Outline each uninfected red blood cell.
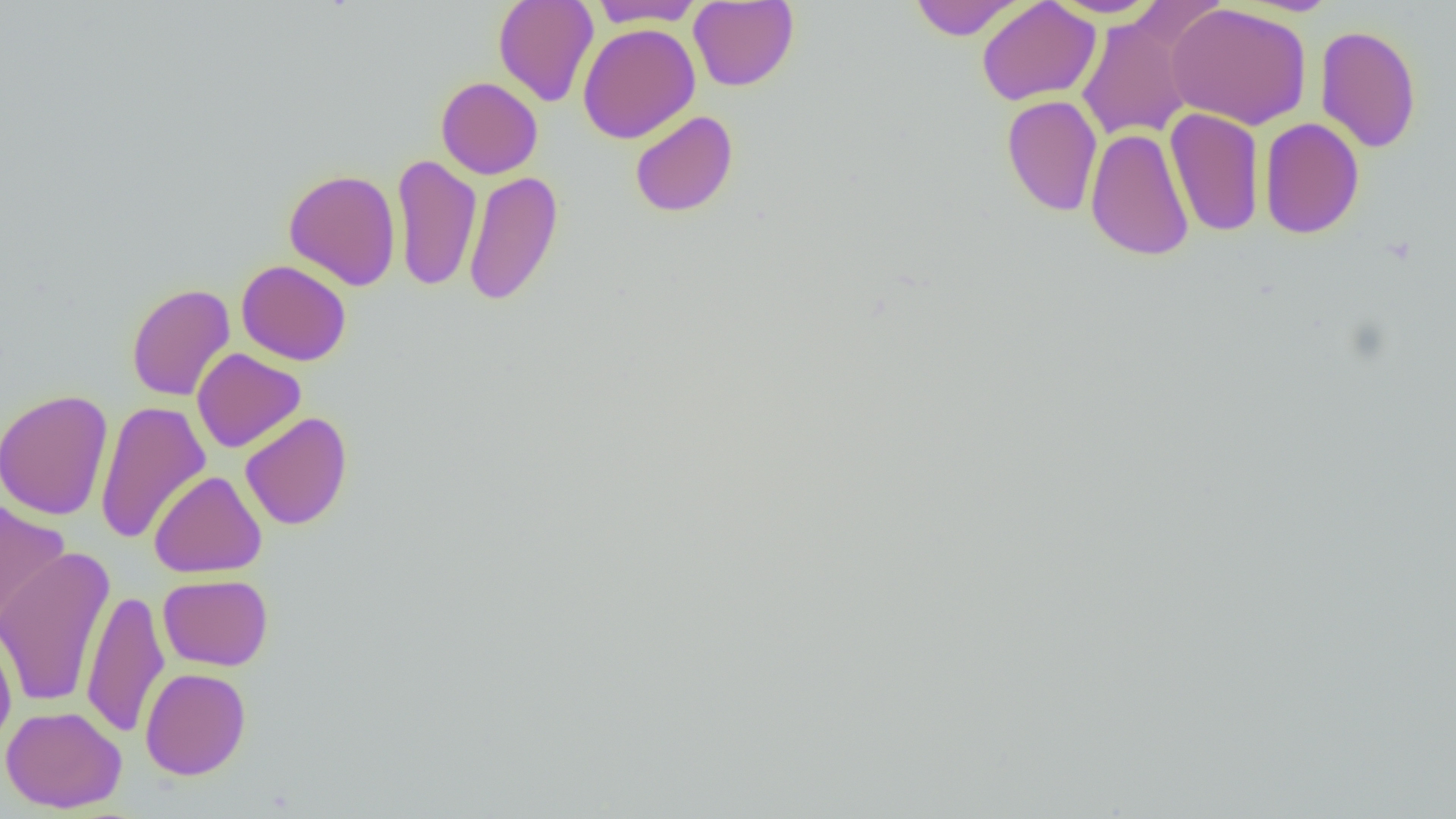
Approximate bounding boxes as (x1, y1, x2, y2) in pixels.
Uninfected red blood cells: (493, 0, 599, 107), (909, 0, 1025, 40), (977, 0, 1100, 106), (1047, 0, 1164, 18), (588, 1, 704, 28), (688, 1, 799, 91), (1166, 3, 1312, 130), (1076, 14, 1195, 141), (578, 23, 700, 143), (1315, 23, 1422, 153), (436, 76, 542, 179), (1002, 95, 1102, 217), (1165, 107, 1265, 237), (630, 110, 738, 217), (1259, 117, 1365, 239), (1085, 127, 1195, 261), (391, 155, 481, 292), (283, 168, 401, 290), (463, 171, 563, 307), (236, 260, 352, 366), (126, 283, 235, 402), (192, 348, 306, 453), (0, 389, 114, 522), (95, 401, 211, 544), (240, 412, 352, 531), (149, 470, 267, 578), (0, 498, 70, 629), (0, 546, 116, 709), (158, 574, 272, 671), (82, 588, 169, 739), (0, 623, 17, 749), (140, 667, 251, 780), (0, 705, 127, 813).

Summary:
  - Slide-level diagnosis: no evidence of blood parasites
  - Field of view: one of a larger specimen
  - Modality: optical microscopy
  - Preparation: thin blood smear
  - Image size: 1456×819 pixels
  - Magnification: 1000x